Identify the parasite.
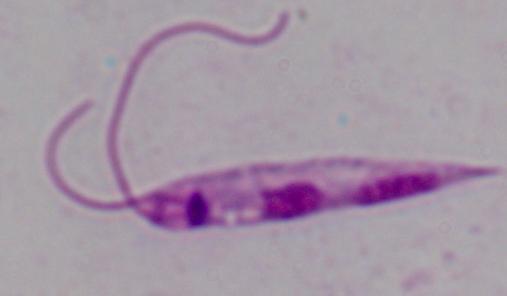

This is Leishmania.

Micrograph. 1000x magnification.